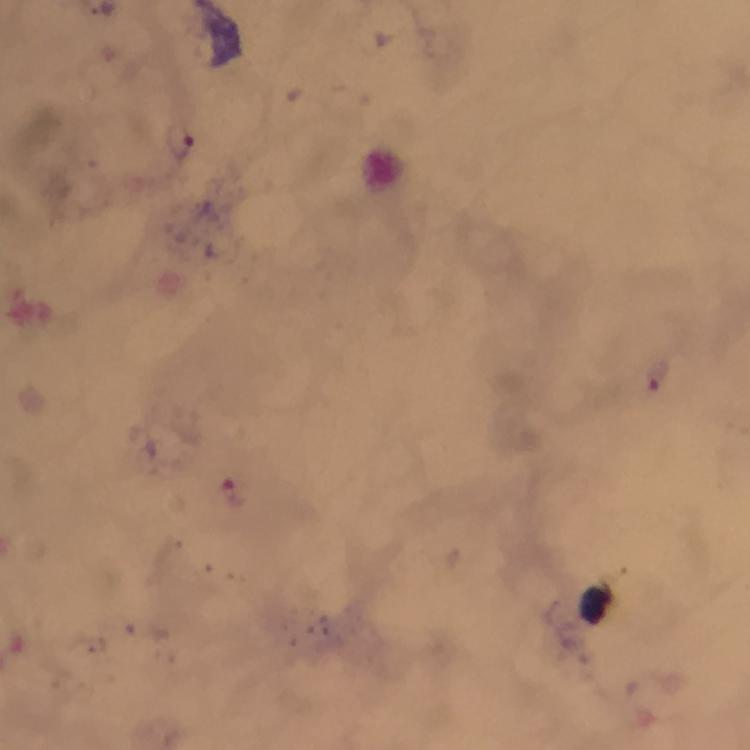

Approximate centers as (x, y) in pixels. Malaria parasite locations: (178, 140), (659, 372), (233, 495). Thick smear. At 100x magnification. Cropped region of a single field of view. From a diagnostic examination for malaria. Image is 750×750 pixels. Photographed through the microscope with a smartphone camera. Giemsa stain. Immersion oil applied.